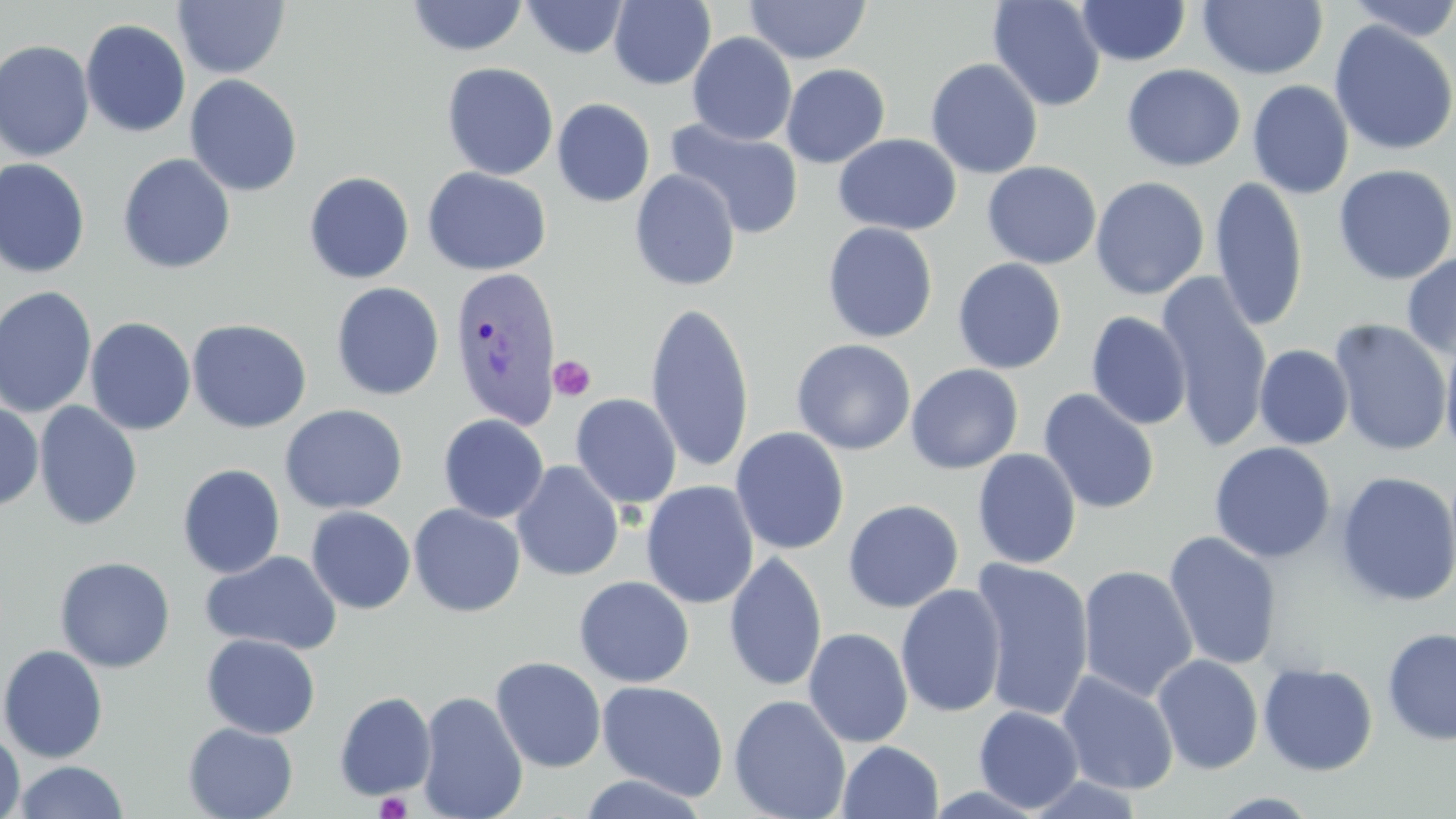

Approximate bounding boxes as named x1/y1/x2/y2 corners in pixels. Plasmodium vivax-infected red blood cell locations: (x1=447, y1=264, x2=562, y2=432). Platelet locations: (x1=549, y1=355, x2=596, y2=401), (x1=375, y1=791, x2=413, y2=819). Uninfected red blood cell locations: (x1=173, y1=0, x2=290, y2=79), (x1=406, y1=0, x2=528, y2=57), (x1=522, y1=0, x2=628, y2=59), (x1=987, y1=0, x2=1106, y2=112), (x1=1342, y1=0, x2=1456, y2=42), (x1=608, y1=1, x2=716, y2=90), (x1=744, y1=1, x2=871, y2=64), (x1=1076, y1=1, x2=1191, y2=66), (x1=1198, y1=1, x2=1328, y2=80), (x1=80, y1=19, x2=191, y2=138), (x1=1328, y1=21, x2=1456, y2=157), (x1=687, y1=32, x2=797, y2=146), (x1=0, y1=40, x2=95, y2=161), (x1=925, y1=58, x2=1043, y2=179), (x1=441, y1=62, x2=559, y2=180), (x1=781, y1=63, x2=890, y2=168), (x1=1121, y1=63, x2=1246, y2=172), (x1=185, y1=74, x2=302, y2=196), (x1=1247, y1=80, x2=1354, y2=199), (x1=552, y1=98, x2=655, y2=208), (x1=664, y1=118, x2=804, y2=239), (x1=833, y1=133, x2=962, y2=235), (x1=117, y1=153, x2=236, y2=274), (x1=0, y1=157, x2=91, y2=279), (x1=982, y1=161, x2=1102, y2=270), (x1=1333, y1=163, x2=1456, y2=285), (x1=422, y1=167, x2=552, y2=276), (x1=629, y1=169, x2=740, y2=291), (x1=304, y1=171, x2=414, y2=284), (x1=1090, y1=176, x2=1210, y2=300), (x1=1210, y1=176, x2=1308, y2=332), (x1=822, y1=222, x2=938, y2=343), (x1=1401, y1=251, x2=1456, y2=361), (x1=952, y1=258, x2=1067, y2=374), (x1=1156, y1=272, x2=1274, y2=452), (x1=331, y1=281, x2=444, y2=401), (x1=0, y1=286, x2=97, y2=418), (x1=645, y1=302, x2=755, y2=476), (x1=1087, y1=311, x2=1192, y2=429), (x1=84, y1=317, x2=197, y2=435), (x1=186, y1=318, x2=313, y2=433), (x1=1329, y1=319, x2=1453, y2=456), (x1=1440, y1=330, x2=1456, y2=462), (x1=791, y1=338, x2=916, y2=455), (x1=1254, y1=344, x2=1354, y2=450), (x1=905, y1=363, x2=1024, y2=474), (x1=1038, y1=388, x2=1160, y2=515), (x1=570, y1=393, x2=682, y2=509), (x1=34, y1=401, x2=142, y2=531), (x1=0, y1=402, x2=44, y2=511), (x1=280, y1=404, x2=408, y2=515), (x1=438, y1=413, x2=549, y2=524), (x1=730, y1=426, x2=850, y2=555), (x1=1209, y1=442, x2=1336, y2=563), (x1=972, y1=448, x2=1082, y2=569), (x1=511, y1=461, x2=624, y2=582), (x1=177, y1=463, x2=286, y2=579), (x1=1335, y1=471, x2=1456, y2=607), (x1=641, y1=481, x2=760, y2=609), (x1=843, y1=499, x2=964, y2=612), (x1=408, y1=503, x2=526, y2=617), (x1=305, y1=506, x2=416, y2=614), (x1=1164, y1=530, x2=1283, y2=671), (x1=201, y1=551, x2=342, y2=655), (x1=723, y1=552, x2=827, y2=692), (x1=54, y1=556, x2=176, y2=672), (x1=969, y1=559, x2=1095, y2=722), (x1=1078, y1=565, x2=1198, y2=702), (x1=574, y1=576, x2=695, y2=687), (x1=895, y1=583, x2=1007, y2=718), (x1=803, y1=627, x2=913, y2=748), (x1=1381, y1=627, x2=1456, y2=745), (x1=201, y1=634, x2=321, y2=740), (x1=0, y1=644, x2=108, y2=763), (x1=1152, y1=653, x2=1264, y2=775), (x1=490, y1=656, x2=607, y2=773), (x1=1258, y1=662, x2=1378, y2=776), (x1=1056, y1=670, x2=1179, y2=795), (x1=596, y1=680, x2=729, y2=800), (x1=334, y1=691, x2=436, y2=800), (x1=417, y1=691, x2=528, y2=819), (x1=729, y1=694, x2=851, y2=819), (x1=974, y1=705, x2=1083, y2=814), (x1=182, y1=722, x2=298, y2=819), (x1=0, y1=728, x2=26, y2=819), (x1=837, y1=741, x2=944, y2=819), (x1=12, y1=760, x2=129, y2=819), (x1=577, y1=773, x2=711, y2=818), (x1=1209, y1=792, x2=1324, y2=817). Slide-level diagnosis: Plasmodium vivax. Thin blood smear. May-Grünwald-Giemsa-stained preparation. Single field of view. Light microscopy. Captured at 1000x magnification. Image is 1456×819 pixels.